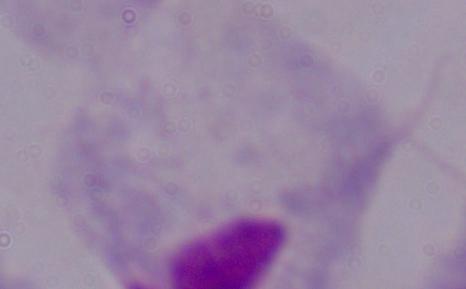 Captured at 1000x magnification. Photomicrograph. A trichomonad is shown.